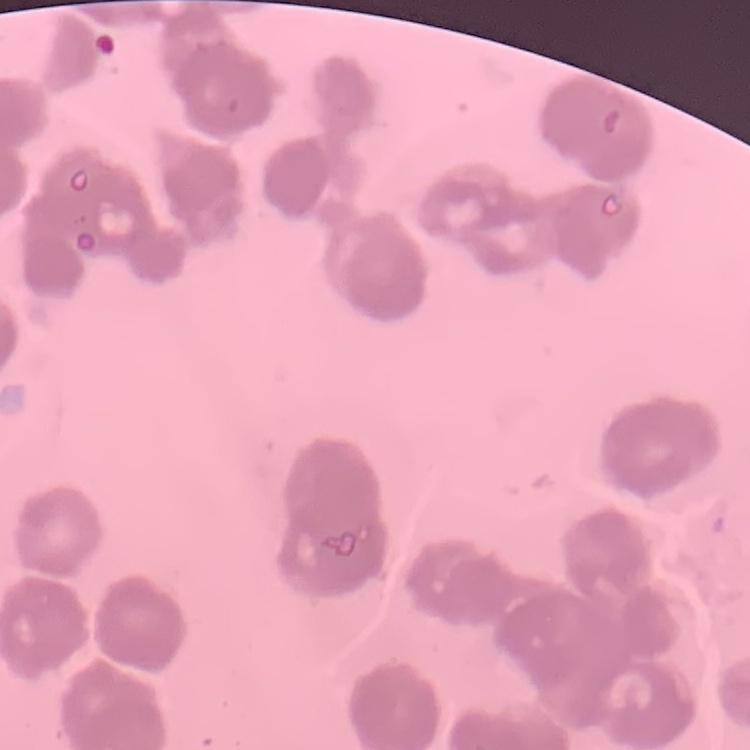

Summary:
  - Erythrocyte morphology: rouleaux formation
  - Stain: Field's or Giemsa
  - Image type: one tile cut from a larger photomicrograph
  - Preparation: thin blood film